Look for Plasmodium parasites.
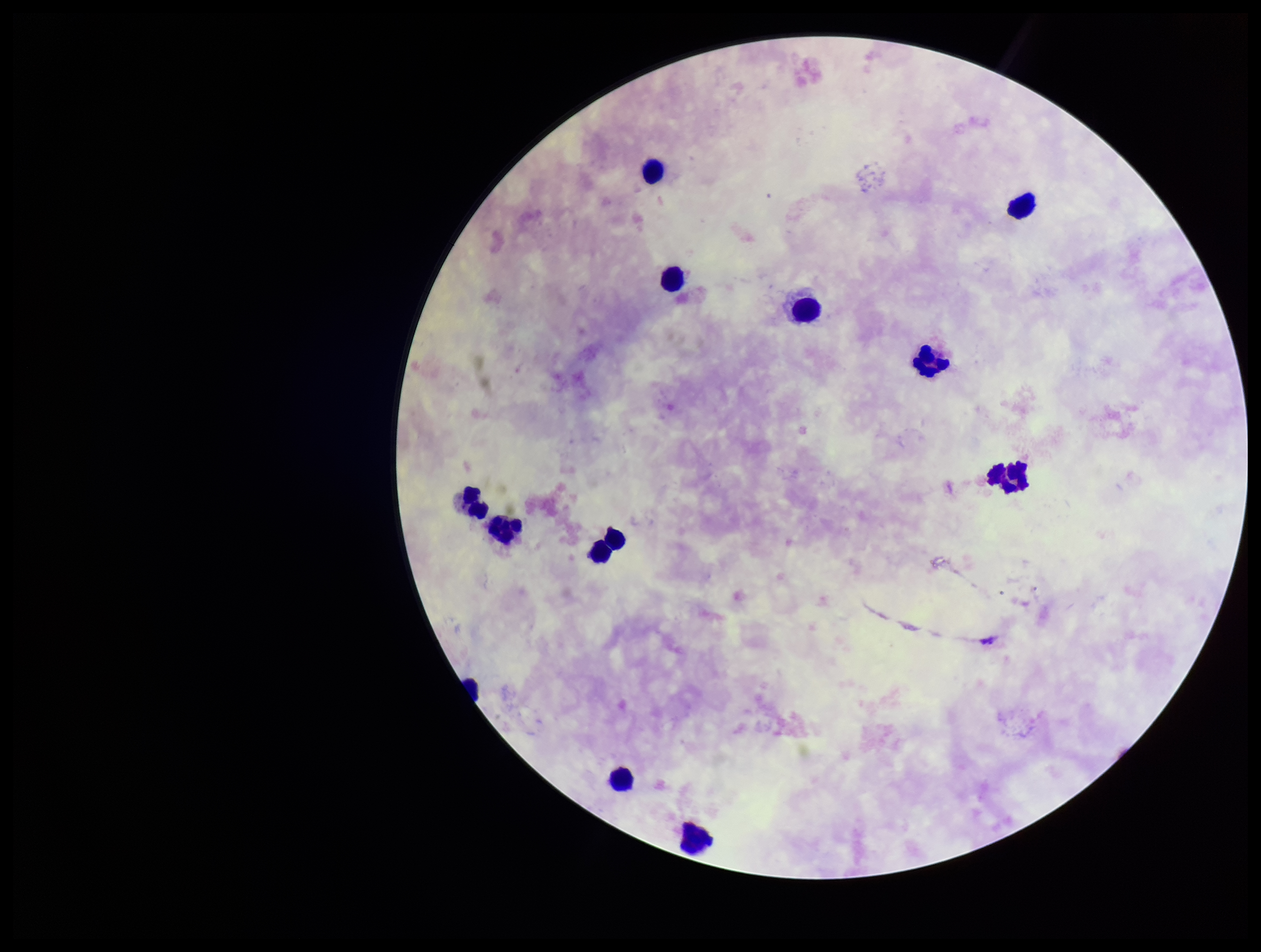
None identified.

capture = smartphone photograph through the microscope eyepiece
image size = 1261×952 pixels
parasite count = 0
stain = Giemsa
preparation = thick
leukocyte count = 13
field of view = single
patient malaria status = negative